State which cell type is depicted.
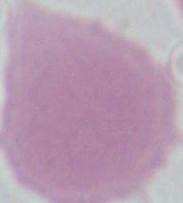

An erythrocyte.

1000x magnification. Micrograph.